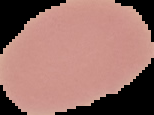 From a thin blood film. Segmented cell region on a black background. Malaria status: uninfected. Image is 154×115 pixels.